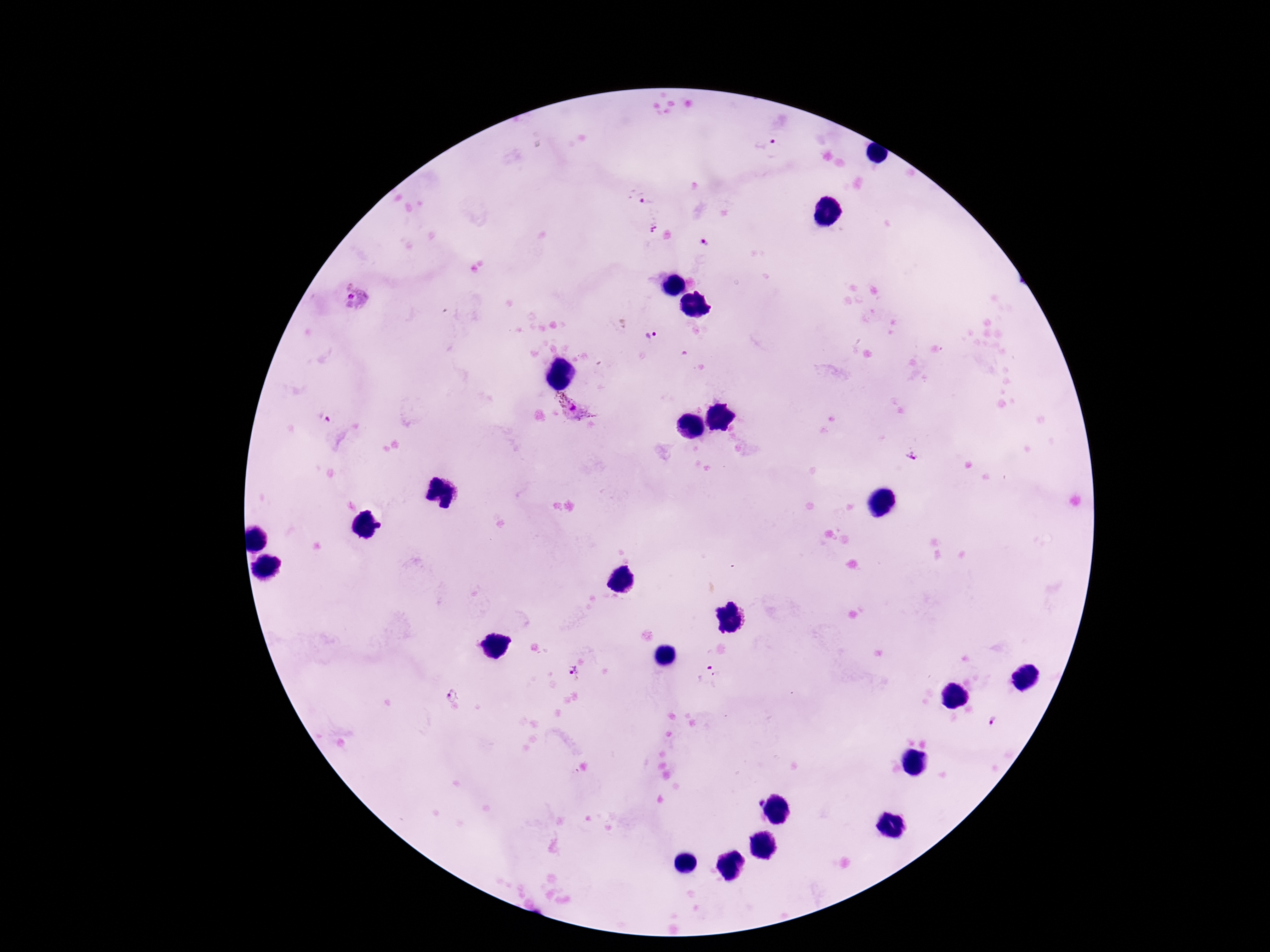
Approximate centers as {x, y} in pixels.
Summary:
  - Plasmodium parasite locations: {765, 150}, {641, 196}, {654, 223}, {706, 243}, {356, 299}, {651, 336}, {575, 411}, {325, 417}, {912, 456}, {574, 673}, {708, 676}, {451, 693}, {993, 723}
  - Image size: 1270×952 pixels
  - Stain: Giemsa
  - Field of view: single
  - Patient malaria status: positive
  - Preparation: thick peripheral-blood smear
  - Magnification: 100x
  - Capture: smartphone camera through the microscope eyepiece